State which parasite is depicted.
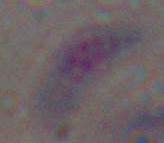

Toxoplasma gondii.

Micrograph. Captured at 1000x magnification.